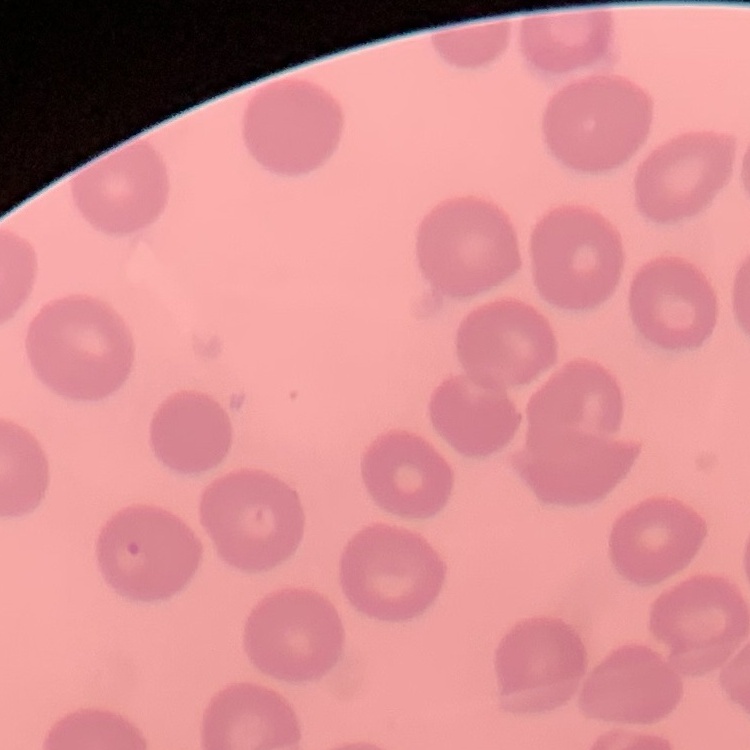

The red blood cells exhibit no rouleaux formation. Thin blood film. One tile cut from a larger photomicrograph. Stained with either Field's or Giemsa.